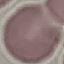 Malaria status: uninfected. Thin blood film. Automatically extracted cell patch, resized to 64 × 64 pixels. Giemsa stain. Photographed with a smartphone camera at the microscope eyepiece.